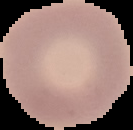
preparation = thin blood smear
image size = 133×130 pixels
image type = segmented cell region on a black background
malaria status = uninfected